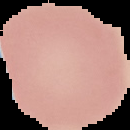
result = negative for Plasmodium parasites
image type = segmented cell region with the area outside set to black
image size = 130×130 pixels
preparation = thin blood smear